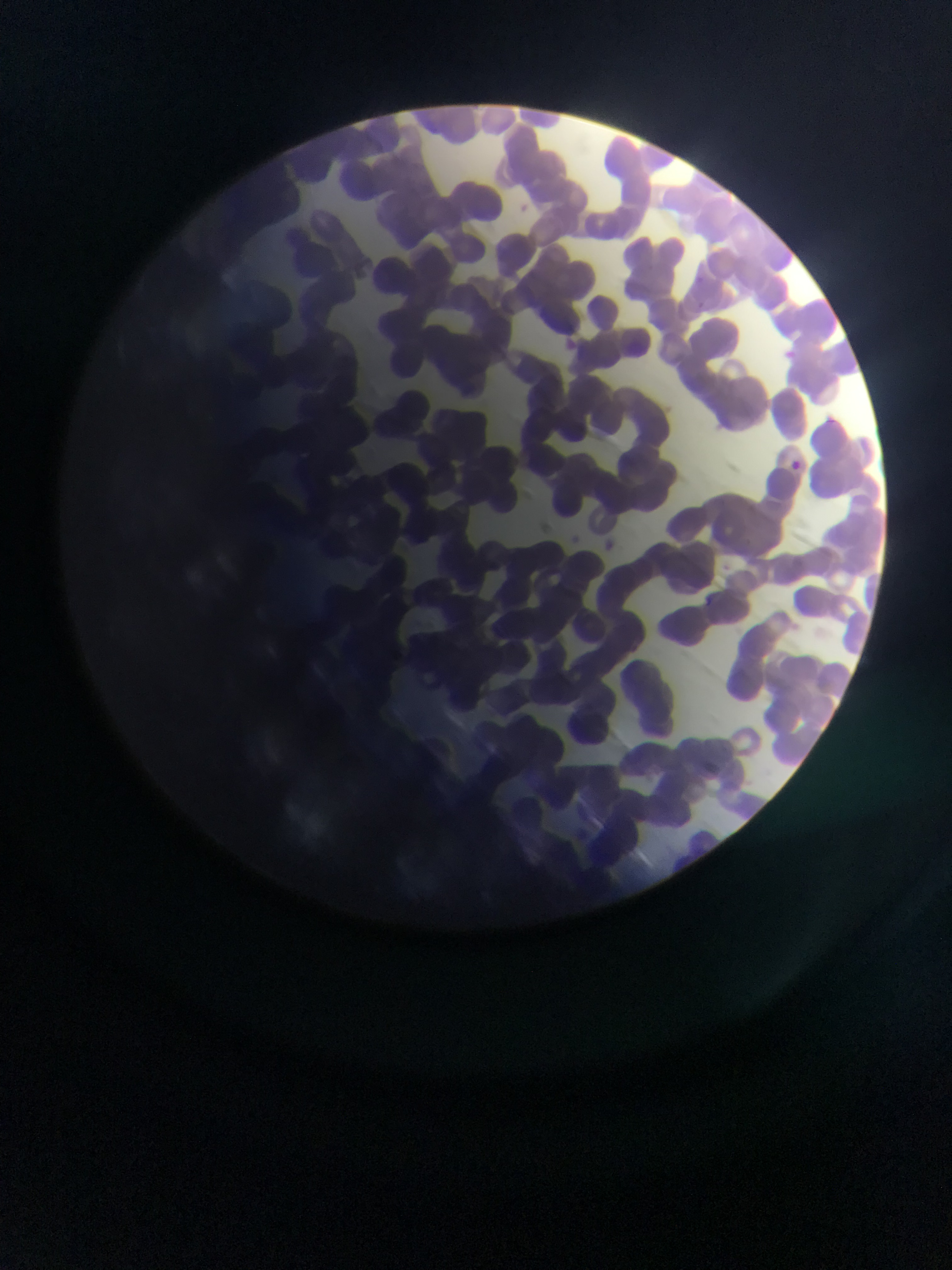 Approximate bounding boxes as (left, top, right, bottom) in pixels. Malaria parasite locations: (825, 408, 835, 426), (790, 456, 811, 475), (702, 596, 712, 606). Image is 952×1270 pixels. Photographed through a microscope with a mobile-phone camera. Collected in Ghana. Thin blood smear. Single field of view.